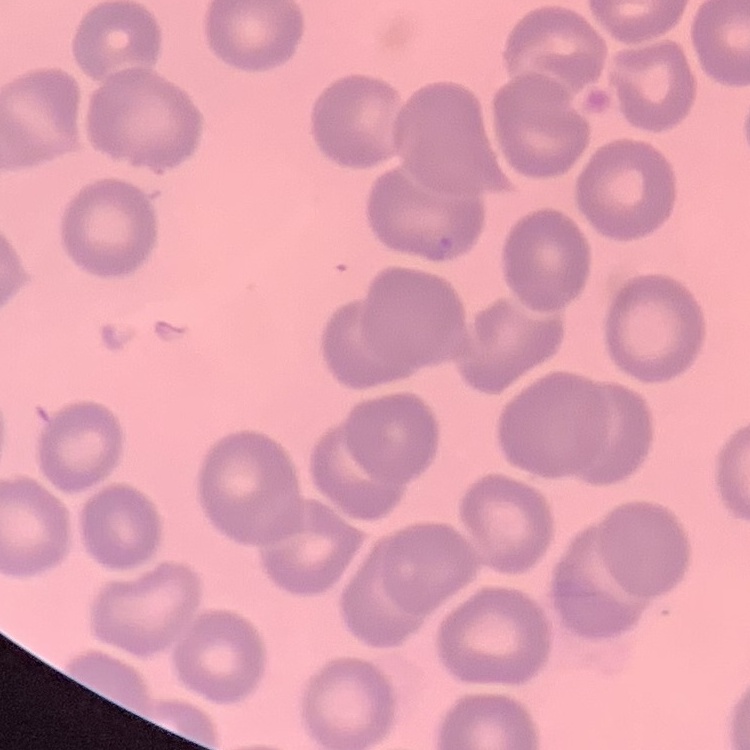 The red blood cells show no rouleaux formation. One tile cut from a larger photomicrograph. Thin peripheral smear. Stained with either Field's or Giemsa.